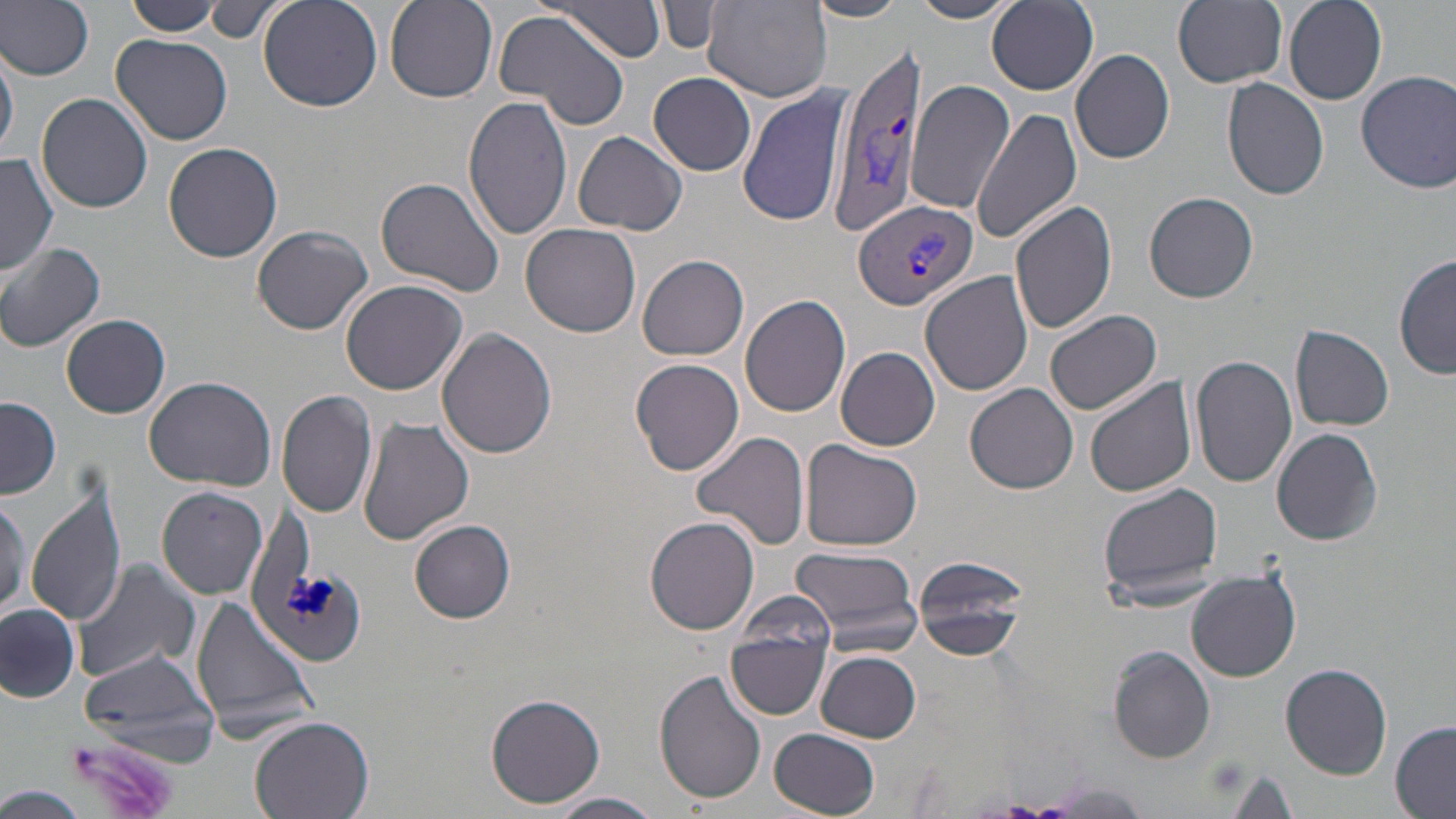
slide-level diagnosis = Plasmodium vivax
uninfected red blood cell locations = approximate bounding boxes as (x1,y1)-(x2,y2) corner pairs in pixels: (0,0)-(96,81), (383,0)-(497,103), (553,0)-(666,62), (804,0)-(909,22), (909,0)-(1015,24), (1173,0)-(1287,88), (1283,0)-(1386,105), (124,1)-(223,36), (258,1)-(383,112), (657,1)-(724,55), (703,1)-(832,104), (988,1)-(1099,94), (207,2)-(277,44), (494,9)-(630,129), (113,33)-(233,145), (0,41)-(17,162), (1069,48)-(1175,165), (1357,69)-(1456,193), (649,73)-(757,175), (907,79)-(1012,216), (1222,79)-(1331,201), (738,86)-(853,229), (37,93)-(153,212), (462,95)-(574,241), (972,106)-(1086,248), (573,132)-(687,236), (163,142)-(283,263), (0,154)-(59,278), (376,175)-(508,300), (1146,191)-(1258,303), (1009,203)-(1118,337), (521,222)-(642,338), (253,224)-(372,335), (0,243)-(106,353), (1395,251)-(1455,380), (639,255)-(749,361), (920,271)-(1034,396), (340,280)-(469,395), (740,295)-(852,417), (1045,309)-(1163,414), (62,314)-(170,418), (1291,326)-(1394,431), (438,331)-(558,460), (836,345)-(941,451), (1189,354)-(1299,489), (630,357)-(744,476), (1084,375)-(1196,499), (144,376)-(278,491), (966,385)-(1079,495), (276,387)-(377,518), (1,397)-(60,499), (358,416)-(475,545), (1272,428)-(1383,546), (691,431)-(811,549), (802,439)-(923,551), (26,478)-(130,631), (1097,481)-(1225,607), (159,487)-(267,599), (0,493)-(27,617), (37,513)-(169,675), (645,517)-(759,636), (410,519)-(516,623), (789,543)-(922,652), (912,556)-(1029,661), (72,557)-(202,685), (1186,569)-(1301,680), (735,586)-(836,673), (191,593)-(318,740), (0,602)-(80,700), (725,621)-(832,722), (78,645)-(224,767), (1108,646)-(1216,763), (814,650)-(921,741), (1280,663)-(1390,778), (655,669)-(767,806), (485,691)-(604,808), (250,715)-(375,819), (1389,720)-(1456,818), (771,729)-(881,818), (1227,770)-(1297,818), (6,788)-(85,819), (548,792)-(665,819)
preparation = thin blood film
image size = 1456×819 pixels
stain = May-Grünwald-Giemsa
modality = optical microscopy
magnification = 1000x
field of view = one of a larger specimen
platelet locations = approximate bounding boxes as (x1,y1)-(x2,y2) corner pairs in pixels: (62,735)-(180,818)
Plasmodium vivax-infected red blood cell locations = approximate bounding boxes as (x1,y1)-(x2,y2) corner pairs in pixels: (826,40)-(931,241), (856,201)-(980,310)